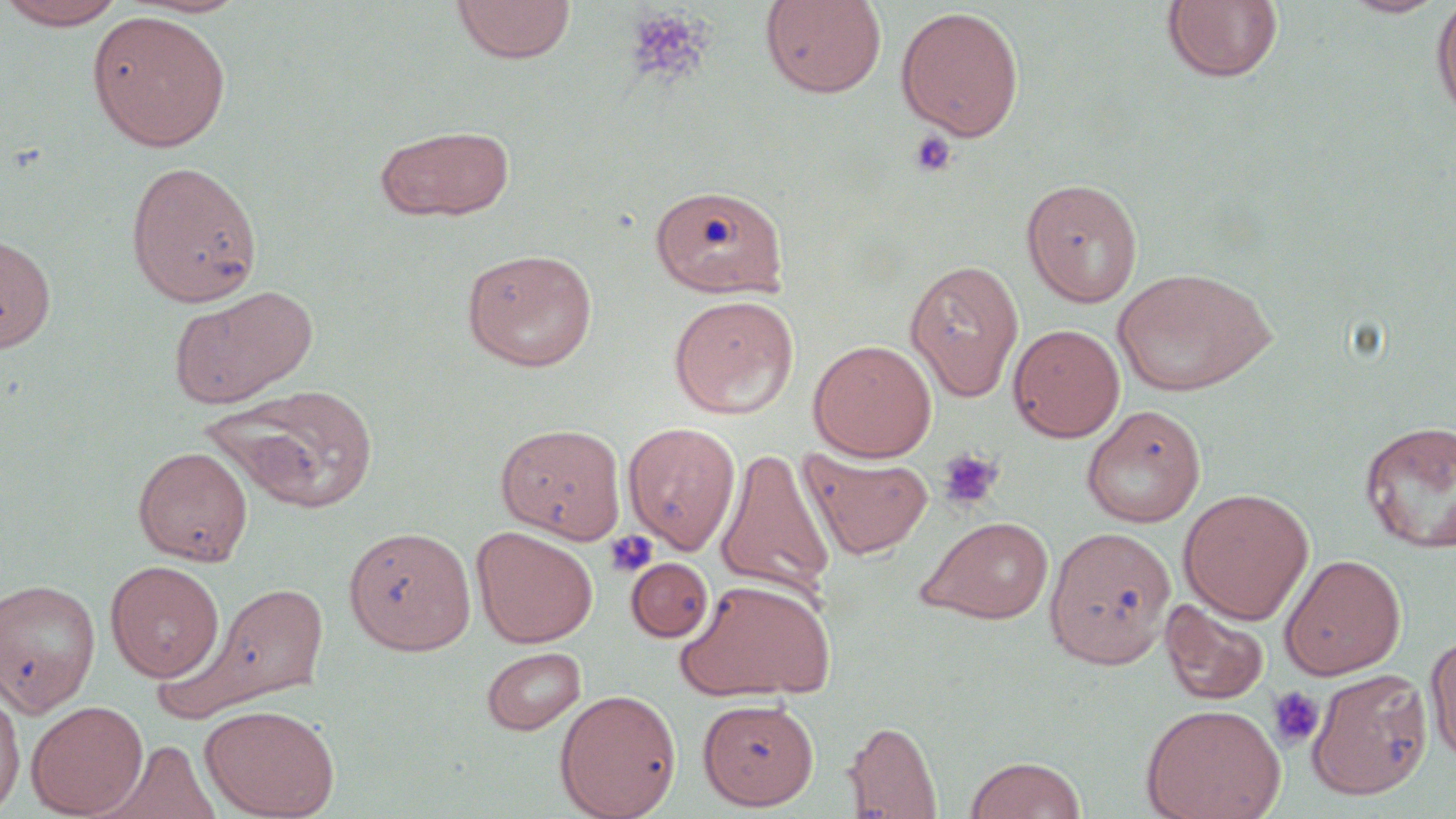
slide_level_diagnosis: negative for blood parasites
preparation: thin blood smear
image_size: 1456×819 pixels
stain: May-Grünwald-Giemsa
field_of_view: single
magnification: 1000x
platelet_locations: 'approximate bounding boxes as (x1,y1)-(x2,y2) corner pairs in pixels: (624,7)-(710,85), (908,130)-(957,178), (937,449)-(1004,512), (604,530)-(659,580), (1267,686)-(1325,750)'
modality: optical microscopy
uninfected_red_blood_cell_locations: 'approximate bounding boxes as (x1,y1)-(x2,y2) corner pairs in pixels: (451,0)-(576,64), (760,0)-(887,99), (1339,0)-(1450,18), (0,1)-(131,29), (1161,1)-(1284,84), (1430,1)-(1456,123), (895,6)-(1025,141), (87,10)-(231,152), (374,124)-(515,221), (125,160)-(263,307), (1021,177)-(1144,307), (650,183)-(789,299), (0,232)-(57,353), (461,247)-(598,371), (905,259)-(1024,401), (1112,267)-(1276,397), (166,285)-(318,409), (667,294)-(800,419), (1008,323)-(1125,442), (808,339)-(937,461), (215,384)-(380,513), (1081,404)-(1206,527), (1358,419)-(1456,553), (622,421)-(742,554), (495,422)-(626,542), (133,446)-(253,564), (715,447)-(835,599), (800,450)-(933,559), (483,454)-(634,625), (1178,488)-(1314,623), (918,516)-(1054,624), (471,525)-(598,648), (343,526)-(476,654), (1045,526)-(1176,668), (1280,553)-(1406,679), (626,557)-(713,641), (105,560)-(225,682), (674,575)-(837,703), (0,578)-(101,716), (172,578)-(332,718), (1160,598)-(1270,706), (1426,634)-(1456,766), (481,646)-(586,736), (1306,668)-(1433,800), (0,685)-(25,817), (554,688)-(682,819), (698,698)-(819,810), (26,699)-(148,817), (199,703)-(339,818), (1140,703)-(1286,819), (843,720)-(943,818), (98,739)-(219,819), (964,756)-(1086,818)'